Name the parasite shown.
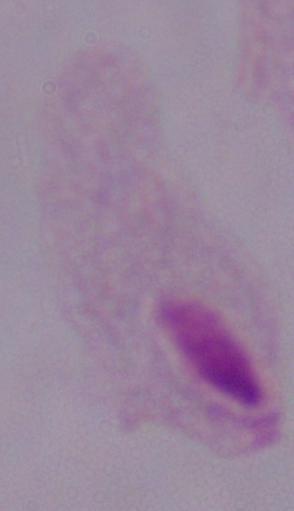

This is a trichomonad.

Photomicrograph. 1000x magnification.